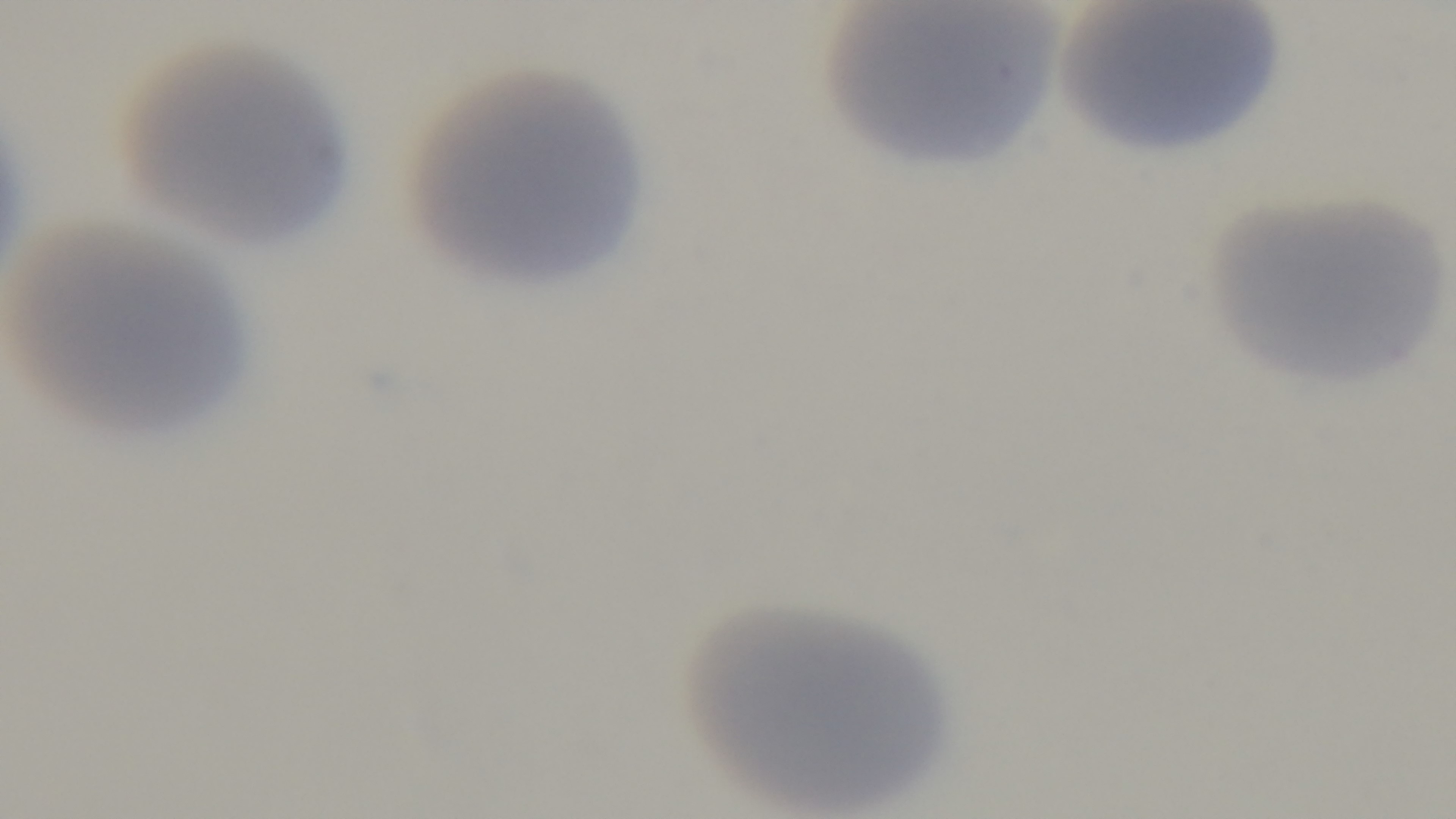
preparation = thin blood film
capture = mounted 4K digital camera
malaria status = uninfected
field of view = one from the slide
stain = Giemsa
objective = 100x oil immersion
modality = light microscopy